Describe the morphology of the erythrocytes.
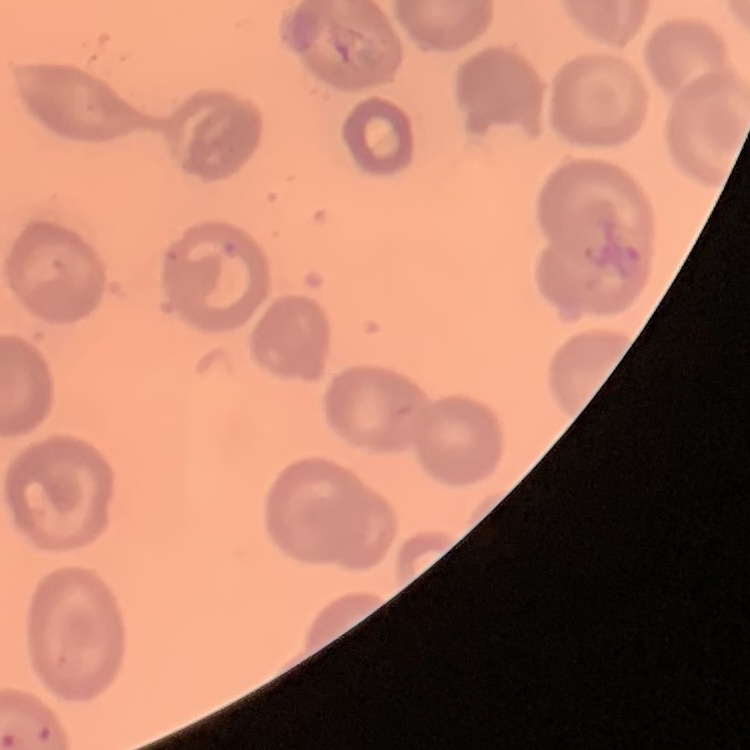

They show no rouleaux formation.

{
  "stain": "Field's or Giemsa",
  "preparation": "thin blood film",
  "image_type": "one tile cut from a larger photomicrograph"
}